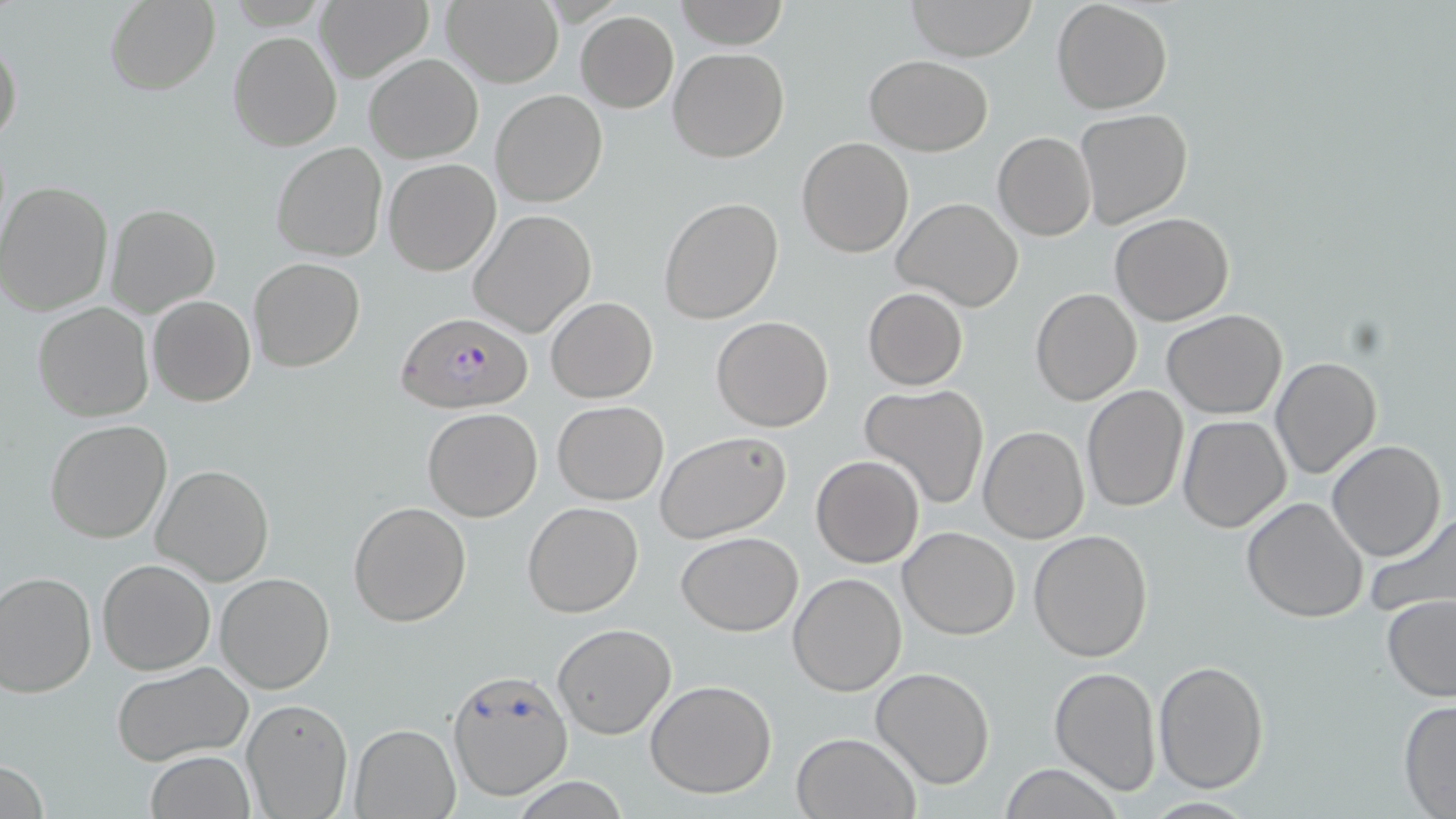 Approximate bounding boxes as [x1, y1, x2, y2] in pixels. Uninfected red blood cell locations: [442, 0, 564, 88], [675, 0, 788, 50], [905, 0, 1038, 61], [1051, 0, 1174, 115], [102, 1, 221, 94], [316, 2, 432, 81], [574, 11, 678, 112], [228, 31, 341, 152], [0, 33, 23, 151], [668, 47, 789, 162], [365, 54, 482, 163], [866, 55, 993, 155], [490, 90, 608, 208], [1074, 109, 1193, 229], [993, 132, 1097, 241], [796, 136, 915, 257], [271, 141, 387, 262], [383, 158, 501, 275], [0, 181, 116, 317], [659, 196, 783, 324], [893, 198, 1023, 312], [105, 203, 221, 318], [468, 208, 599, 339], [1110, 212, 1235, 326], [248, 257, 366, 373], [1031, 287, 1142, 405], [862, 288, 968, 391], [147, 296, 256, 406], [545, 296, 657, 403], [33, 302, 155, 421], [1162, 308, 1288, 420], [711, 315, 834, 431], [1270, 355, 1381, 477], [860, 384, 989, 510], [1081, 386, 1189, 514], [552, 401, 668, 505], [421, 407, 543, 522], [1177, 416, 1291, 534], [45, 418, 172, 543], [979, 426, 1089, 543], [655, 430, 792, 543], [1326, 440, 1445, 562], [811, 455, 924, 567], [152, 464, 275, 586], [1241, 498, 1369, 624], [522, 501, 644, 618], [348, 502, 471, 627], [1366, 509, 1456, 623], [900, 526, 1019, 639], [1028, 529, 1153, 663], [675, 531, 803, 636], [98, 558, 214, 675], [0, 571, 97, 698], [214, 572, 337, 694], [789, 572, 906, 695], [1381, 594, 1456, 702], [551, 622, 677, 739], [112, 659, 254, 765], [1152, 659, 1270, 792], [1048, 665, 1161, 795], [871, 667, 996, 790], [447, 668, 574, 799], [645, 679, 777, 798], [241, 697, 353, 818], [1398, 700, 1456, 817], [350, 723, 460, 817], [792, 731, 919, 818], [144, 750, 255, 819], [997, 764, 1127, 819], [513, 777, 629, 818]. Plasmodium falciparum-infected red blood cell locations: [397, 310, 530, 413]. Slide-level diagnosis: Plasmodium falciparum. Light microscopy. One field of a larger specimen. Image is 1456×819 pixels. 1000x magnification. May-Grünwald-Giemsa-stained preparation. Thin blood smear.